Report the malaria status of this cell.
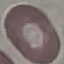

Uninfected.

Cell patch, automatically extracted from a larger field of view and resized to 64 × 64 pixels. Giemsa-stained preparation. Photographed with a smartphone camera at the microscope eyepiece. Thin blood smear.